Report the malaria status of this cell.
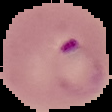
It is parasitized.

image size = 112×112 pixels
preparation = thin blood film
image type = segmented cell region with the area outside set to black